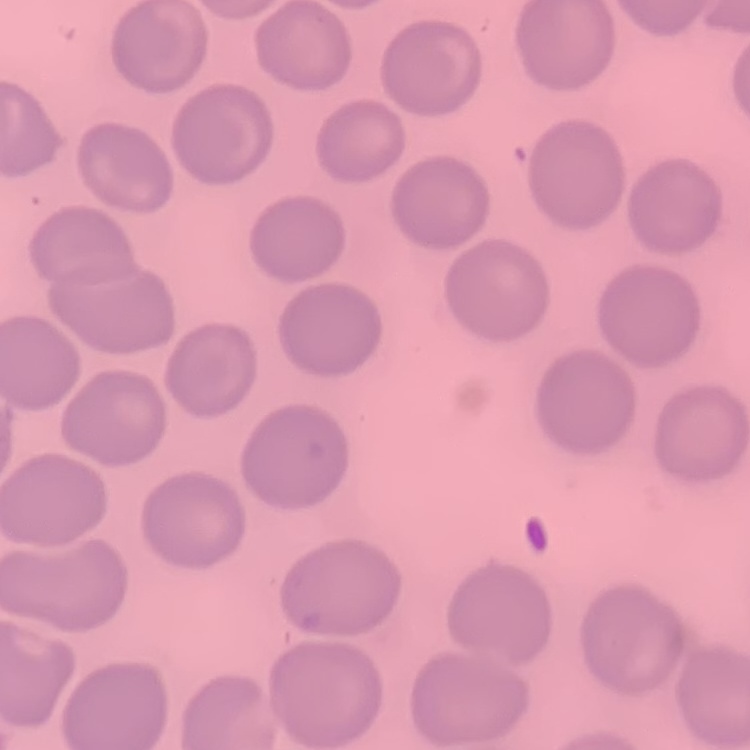

Summary:
  - Red blood cell morphology: no rouleaux formation
  - Preparation: thin blood film
  - Stain: Field's or Giemsa
  - Image type: square crop of a larger photomicrograph